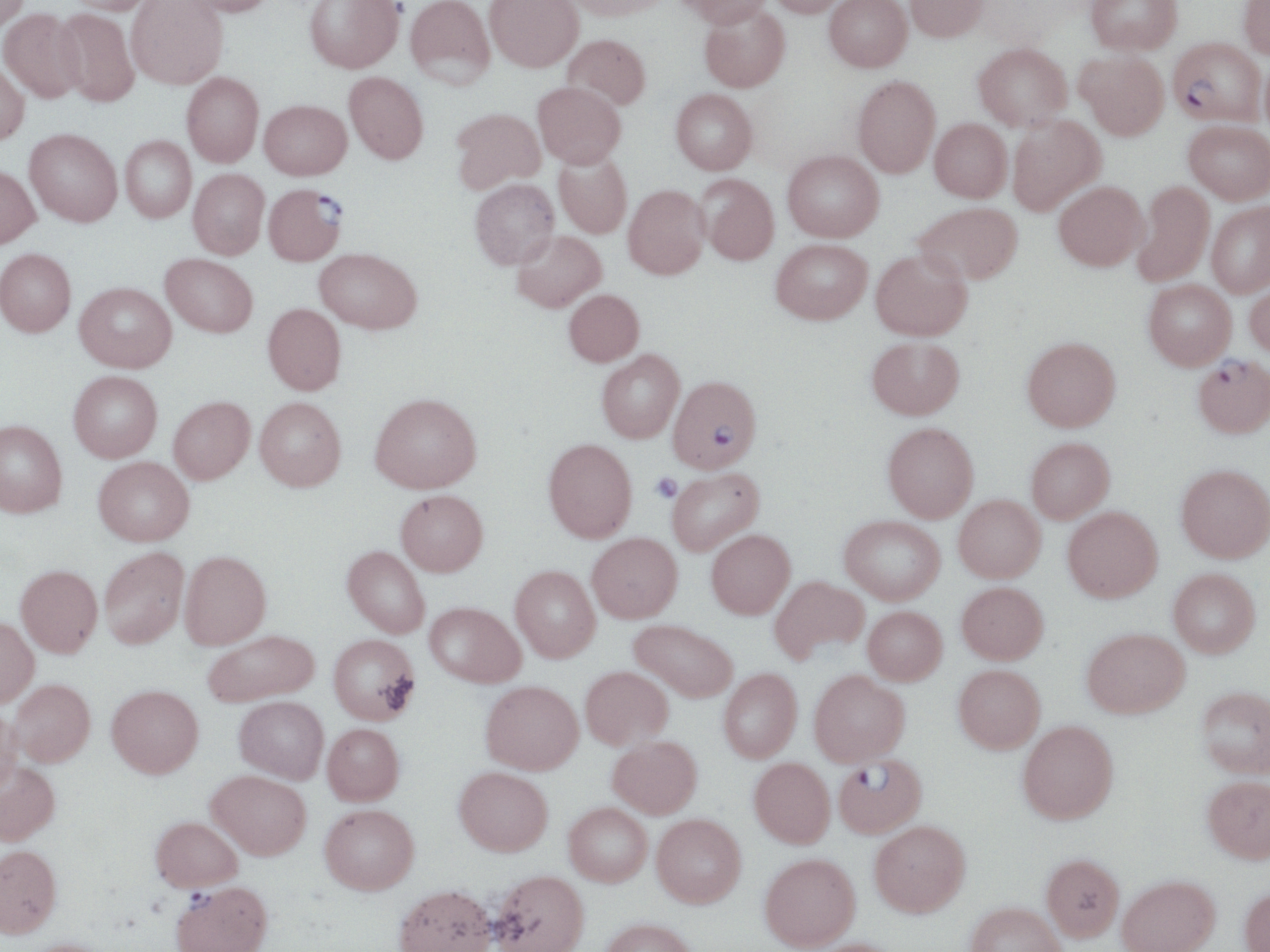
slide-level diagnosis = Plasmodium falciparum
platelet locations = approximate bounding boxes as (x1, y1, x2, y2) in pixels: (650, 472, 682, 502)
image size = 1270×952 pixels
preparation = thin blood film
magnification = 1000x
Plasmodium falciparum-infected red blood cell locations = approximate bounding boxes as (x1, y1, x2, y2) in pixels: (1169, 37, 1265, 125), (264, 184, 347, 266), (1193, 355, 1270, 437), (668, 375, 761, 473), (834, 755, 926, 839), (170, 881, 272, 952)
field of view = single
uninfected red blood cell locations = approximate bounding boxes as (x1, y1, x2, y2) in pixels: (0, 0, 30, 33), (63, 0, 158, 16), (127, 0, 227, 89), (178, 0, 275, 18), (305, 0, 404, 75), (405, 0, 495, 89), (485, 0, 583, 72), (562, 0, 671, 20), (676, 0, 773, 28), (766, 0, 848, 17), (824, 0, 912, 72), (904, 0, 990, 42), (1085, 0, 1182, 54), (1238, 0, 1270, 59), (699, 5, 790, 92), (54, 8, 140, 108), (0, 9, 86, 103), (563, 34, 651, 111), (973, 42, 1072, 130), (1074, 50, 1170, 140), (1261, 52, 1270, 141), (0, 61, 30, 146), (181, 72, 263, 167), (344, 73, 428, 166), (852, 76, 940, 178), (533, 81, 626, 169), (671, 89, 758, 175), (259, 101, 352, 180), (450, 108, 545, 193), (1007, 115, 1106, 215), (930, 118, 1012, 202), (1184, 120, 1270, 203), (25, 129, 122, 226), (120, 136, 196, 222), (782, 150, 884, 242), (553, 151, 632, 239), (0, 165, 40, 248), (188, 168, 269, 259), (697, 174, 779, 265), (470, 179, 559, 269), (1054, 181, 1148, 270), (1132, 181, 1215, 287), (623, 185, 710, 279), (1207, 201, 1270, 297), (915, 202, 1023, 284), (512, 230, 606, 312), (771, 239, 872, 324), (315, 248, 422, 334), (0, 249, 76, 337), (871, 249, 972, 340), (161, 254, 258, 337), (1246, 276, 1270, 360), (1143, 280, 1237, 370), (74, 282, 176, 372), (564, 289, 644, 366), (263, 303, 346, 394), (867, 336, 964, 420), (1022, 337, 1121, 432), (597, 350, 685, 442), (68, 371, 162, 462), (370, 392, 481, 492), (169, 397, 255, 484), (255, 397, 346, 490), (0, 420, 67, 517), (882, 422, 979, 521), (1026, 437, 1115, 523), (543, 438, 637, 542), (94, 456, 194, 545), (1176, 464, 1270, 562), (667, 468, 764, 556), (396, 489, 488, 576), (954, 495, 1045, 582), (1063, 507, 1163, 602), (840, 515, 945, 604), (706, 530, 795, 619), (587, 533, 682, 622), (343, 546, 431, 638), (99, 547, 189, 648), (180, 550, 271, 648), (16, 565, 102, 656), (510, 565, 600, 662), (1168, 569, 1260, 657), (770, 576, 868, 662), (957, 581, 1048, 664), (425, 602, 525, 687), (863, 606, 947, 685), (0, 617, 38, 707), (630, 619, 738, 702), (1082, 627, 1190, 717), (203, 630, 319, 706), (329, 634, 420, 724), (953, 664, 1045, 753), (580, 666, 672, 749), (719, 669, 802, 762), (809, 669, 910, 765), (9, 678, 95, 766), (480, 681, 583, 774), (107, 684, 203, 777), (1197, 687, 1270, 778), (235, 696, 328, 783), (0, 706, 21, 795), (1017, 720, 1119, 823), (322, 723, 404, 805), (608, 735, 702, 818), (749, 758, 836, 847), (0, 761, 60, 845), (454, 766, 553, 855), (207, 770, 311, 859), (1203, 775, 1270, 863), (564, 802, 653, 885), (320, 804, 419, 893), (651, 814, 746, 907), (151, 816, 241, 892), (869, 821, 970, 916), (0, 845, 62, 937), (760, 853, 861, 950), (1041, 854, 1124, 941), (488, 869, 589, 952), (1117, 876, 1220, 952), (394, 885, 495, 951), (1238, 886, 1270, 951), (965, 902, 1068, 952), (598, 918, 698, 952), (18, 938, 118, 952), (800, 938, 904, 952)
stain = May-Grünwald-Giemsa
modality = optical microscopy